Comment on the morphology of the erythrocytes.
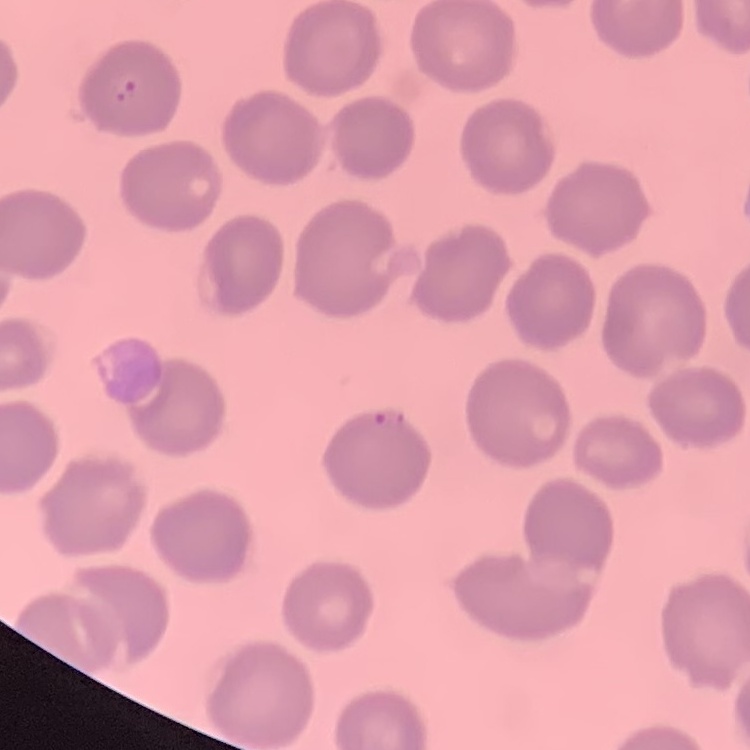

They show no rouleaux formation.

Stained with either Field's or Giemsa. Thin blood smear. Square crop of a larger photomicrograph.